Name the blood parasite species.
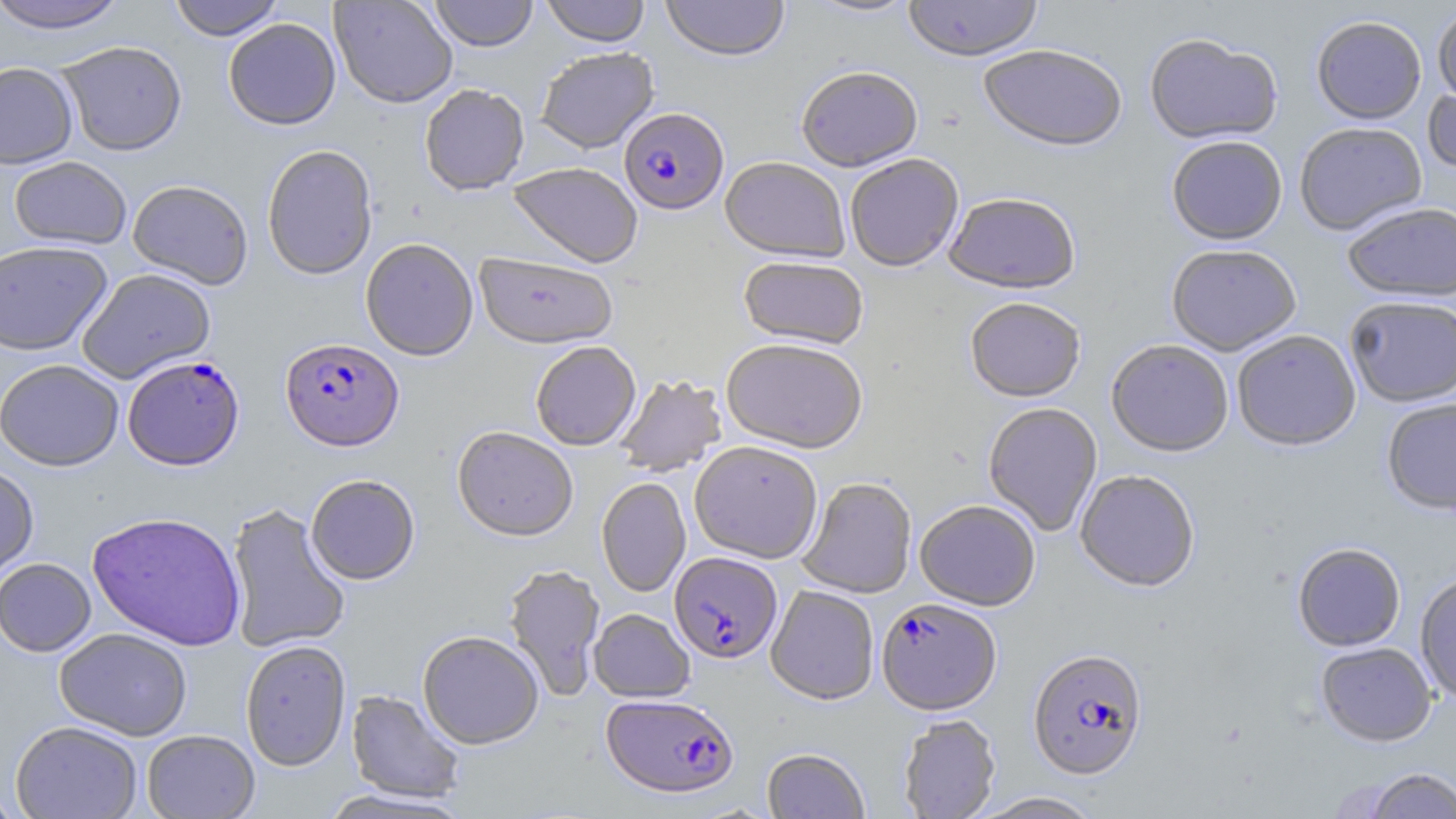

Plasmodium falciparum.

preparation = thin blood film
Plasmodium falciparum-infected red blood cell locations = approximate bounding boxes as [x1, y1, x2, y2] in pixels: [619, 109, 729, 217], [280, 338, 405, 452], [122, 355, 245, 471], [669, 553, 782, 665], [874, 600, 999, 717], [1027, 651, 1148, 783], [601, 695, 739, 801]
field of view = single
uninfected red blood cell locations = approximate bounding boxes as [x1, y1, x2, y2] in pixels: [167, 0, 284, 41], [329, 0, 458, 109], [429, 0, 538, 52], [541, 0, 650, 48], [661, 0, 789, 63], [804, 0, 920, 19], [903, 0, 1043, 64], [0, 1, 130, 34], [1433, 7, 1456, 111], [224, 18, 341, 131], [1312, 18, 1426, 127], [1145, 35, 1283, 148], [57, 41, 188, 156], [978, 47, 1127, 156], [536, 48, 659, 155], [0, 62, 79, 169], [797, 69, 923, 175], [1423, 84, 1456, 180], [419, 85, 530, 198], [1295, 124, 1427, 237], [1167, 138, 1287, 248], [262, 146, 378, 281], [9, 156, 131, 250], [846, 157, 964, 274], [720, 159, 849, 265], [507, 164, 643, 270], [127, 179, 253, 290], [944, 196, 1081, 297], [1343, 204, 1456, 305], [360, 239, 478, 362], [0, 240, 113, 356], [1166, 247, 1302, 358], [475, 254, 617, 351], [738, 258, 868, 351], [77, 268, 216, 383], [1345, 299, 1456, 409], [965, 300, 1085, 404], [1232, 332, 1361, 453], [721, 341, 868, 455], [1106, 342, 1233, 459], [531, 343, 641, 452], [0, 359, 124, 471], [614, 375, 727, 477], [1381, 400, 1456, 517], [983, 403, 1103, 537], [451, 428, 578, 543], [689, 444, 823, 565], [0, 463, 39, 580], [1075, 472, 1200, 594], [305, 475, 420, 585], [596, 478, 691, 597], [798, 478, 917, 599], [915, 501, 1041, 612], [226, 503, 351, 654], [87, 511, 247, 651], [1293, 545, 1406, 653], [0, 558, 96, 657], [503, 565, 606, 702], [1414, 574, 1456, 707], [766, 586, 879, 706], [589, 609, 695, 703], [54, 628, 193, 741], [418, 632, 544, 750], [240, 641, 351, 771], [1317, 644, 1436, 748], [346, 690, 465, 804], [898, 715, 1001, 819], [11, 720, 143, 819], [142, 730, 260, 818], [762, 748, 870, 819], [1363, 768, 1456, 819], [0, 785, 26, 818], [316, 788, 474, 818], [972, 793, 1105, 819]
stain = May-Grünwald-Giemsa
magnification = 1000x
image size = 1456×819 pixels
modality = optical microscopy